State the blood parasite species.
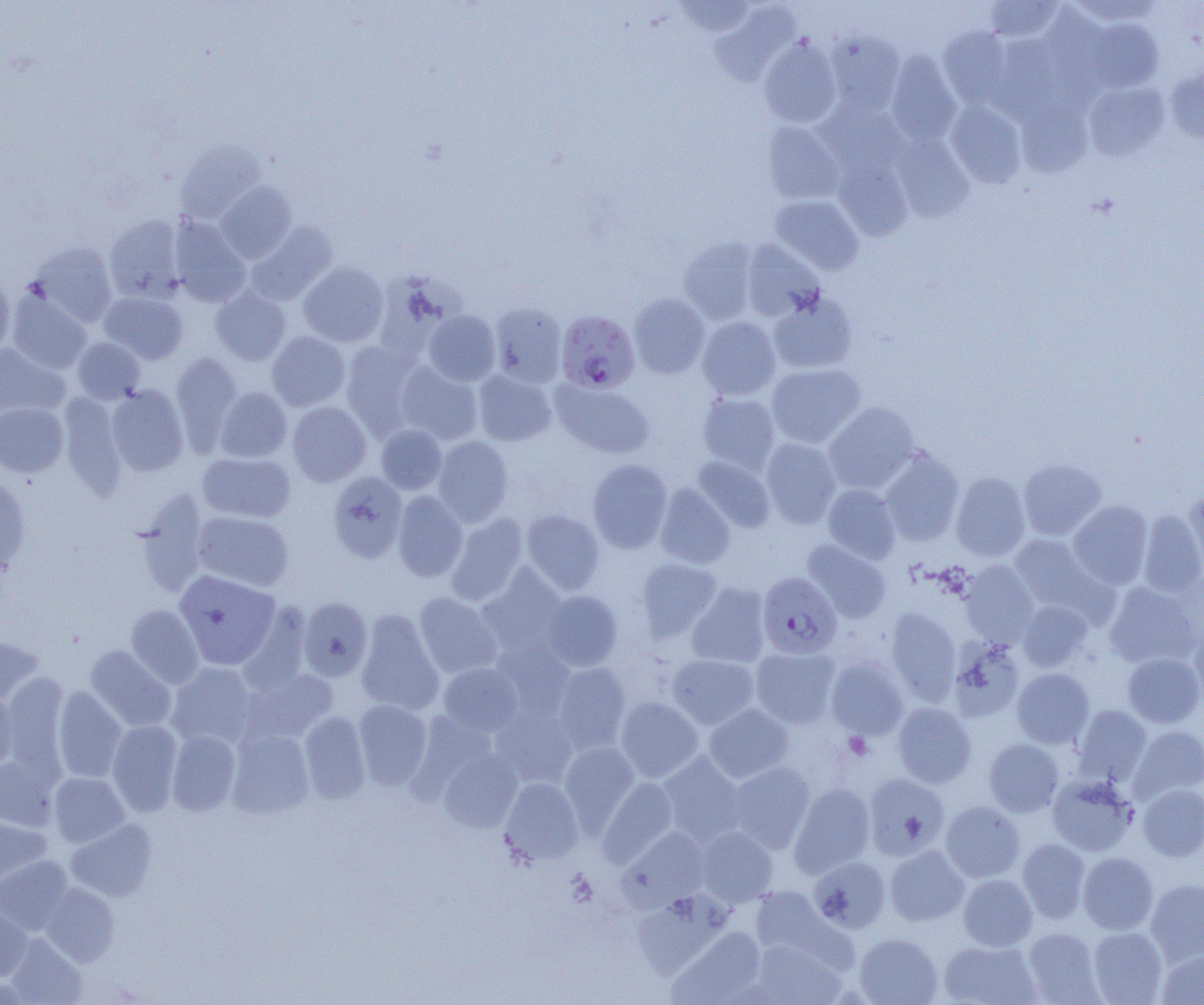

Plasmodium falciparum.

modality = optical microscopy
uninfected red blood cell locations = approximate bounding boxes as (x1,y1)-(x2,y2) corner pairs in pixels: (675,0)-(755,38), (984,0)-(1064,44), (1067,0)-(1164,26), (711,4)-(798,86), (1083,19)-(1163,92), (939,27)-(1015,109), (826,29)-(906,116), (992,34)-(1067,119), (759,37)-(842,127), (885,51)-(962,146), (1166,66)-(1204,143), (1083,81)-(1170,161), (1017,99)-(1093,178), (945,100)-(1026,188), (815,102)-(908,177), (761,122)-(846,205), (890,133)-(974,221), (174,140)-(266,223), (832,155)-(912,240), (215,181)-(297,263), (770,194)-(864,275), (104,215)-(186,302), (168,216)-(251,307), (246,221)-(337,304), (679,237)-(759,324), (740,239)-(825,321), (29,241)-(118,326), (298,262)-(388,347), (0,274)-(14,357), (211,288)-(291,366), (7,291)-(92,373), (100,291)-(188,364), (628,293)-(710,379), (768,293)-(857,374), (489,302)-(567,387), (423,309)-(501,385), (697,316)-(781,400), (267,332)-(350,411), (73,337)-(145,403), (340,341)-(422,438), (0,344)-(68,419), (171,353)-(243,453), (395,362)-(482,445), (765,362)-(865,448), (473,370)-(557,446), (552,381)-(654,459), (106,385)-(188,476), (214,387)-(292,462), (697,392)-(781,475), (59,393)-(128,499), (287,401)-(371,487), (0,402)-(68,477), (823,402)-(920,494), (375,424)-(447,494), (432,435)-(513,526), (760,437)-(842,529), (879,448)-(965,547), (198,452)-(295,522), (692,456)-(775,532), (1018,458)-(1107,540), (587,459)-(672,553), (327,471)-(407,563), (950,472)-(1031,561), (0,474)-(31,572), (654,483)-(735,568), (822,483)-(902,564), (1184,490)-(1204,572), (132,491)-(209,599), (393,491)-(467,581), (1068,500)-(1153,588), (521,510)-(605,595), (193,511)-(294,591), (1137,511)-(1204,597), (445,513)-(529,605), (1008,533)-(1102,614), (802,540)-(891,623), (635,557)-(722,640), (959,560)-(1040,647), (476,565)-(568,657), (174,569)-(281,670), (1104,581)-(1200,669), (687,583)-(772,668), (541,590)-(622,671), (413,592)-(502,678), (297,596)-(373,680), (1017,600)-(1093,672), (125,604)-(204,688), (885,608)-(961,704), (356,611)-(444,715), (1188,620)-(1204,706), (0,636)-(44,706), (949,638)-(1026,722), (490,639)-(575,721), (84,645)-(176,732), (750,646)-(840,728), (1122,652)-(1204,728), (667,654)-(759,729), (826,656)-(909,740), (166,662)-(258,749), (438,662)-(522,736), (551,662)-(631,753), (240,666)-(338,744), (1012,667)-(1095,749), (2,675)-(68,773), (52,686)-(127,783), (0,691)-(18,774), (615,696)-(703,782), (353,700)-(432,789), (892,702)-(976,788), (703,704)-(793,783), (1072,705)-(1152,784), (491,708)-(577,787), (299,712)-(370,804), (107,720)-(183,816), (1128,725)-(1204,803), (227,729)-(314,818), (166,730)-(241,816), (984,738)-(1064,816), (559,741)-(639,828), (437,747)-(523,832), (658,753)-(746,844), (0,756)-(59,830), (725,762)-(816,852), (48,772)-(130,847), (863,773)-(950,859), (1047,774)-(1138,856), (499,778)-(583,865), (598,778)-(679,866), (789,783)-(876,877), (1138,784)-(1204,861), (940,801)-(1025,882), (0,811)-(52,886), (65,819)-(157,902), (620,826)-(710,910), (695,826)-(778,907), (1017,839)-(1090,922), (885,845)-(969,926), (1078,851)-(1158,935), (0,856)-(73,934), (809,856)-(891,933), (958,874)-(1037,951), (1145,878)-(1204,965), (41,883)-(119,966), (750,886)-(832,961), (632,891)-(733,979), (0,907)-(34,980), (667,926)-(766,1004), (1087,926)-(1168,1004), (1023,927)-(1103,1004), (5,933)-(88,1003), (854,933)-(942,1005), (749,939)-(846,1004), (938,940)-(1041,1005), (1157,948)-(1204,1004)
preparation = thin blood film
image size = 1204×1005 pixels
field of view = single
Plasmodium falciparum-infected red blood cell locations = approximate bounding boxes as (x1,y1)-(x2,y2) corner pairs in pixels: (556,310)-(640,394), (757,571)-(842,658)
magnification = 1000x
platelet locations = approximate bounding boxes as (x1,y1)-(x2,y2) corner pairs in pixels: (843,732)-(873,760)